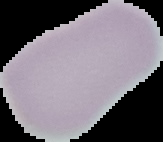
image type = cell region segmented out of the field of view; surrounding area masked to black
result = negative for Plasmodium parasites
preparation = thin blood smear
image size = 163×142 pixels